Outline each uninfected red blood cell.
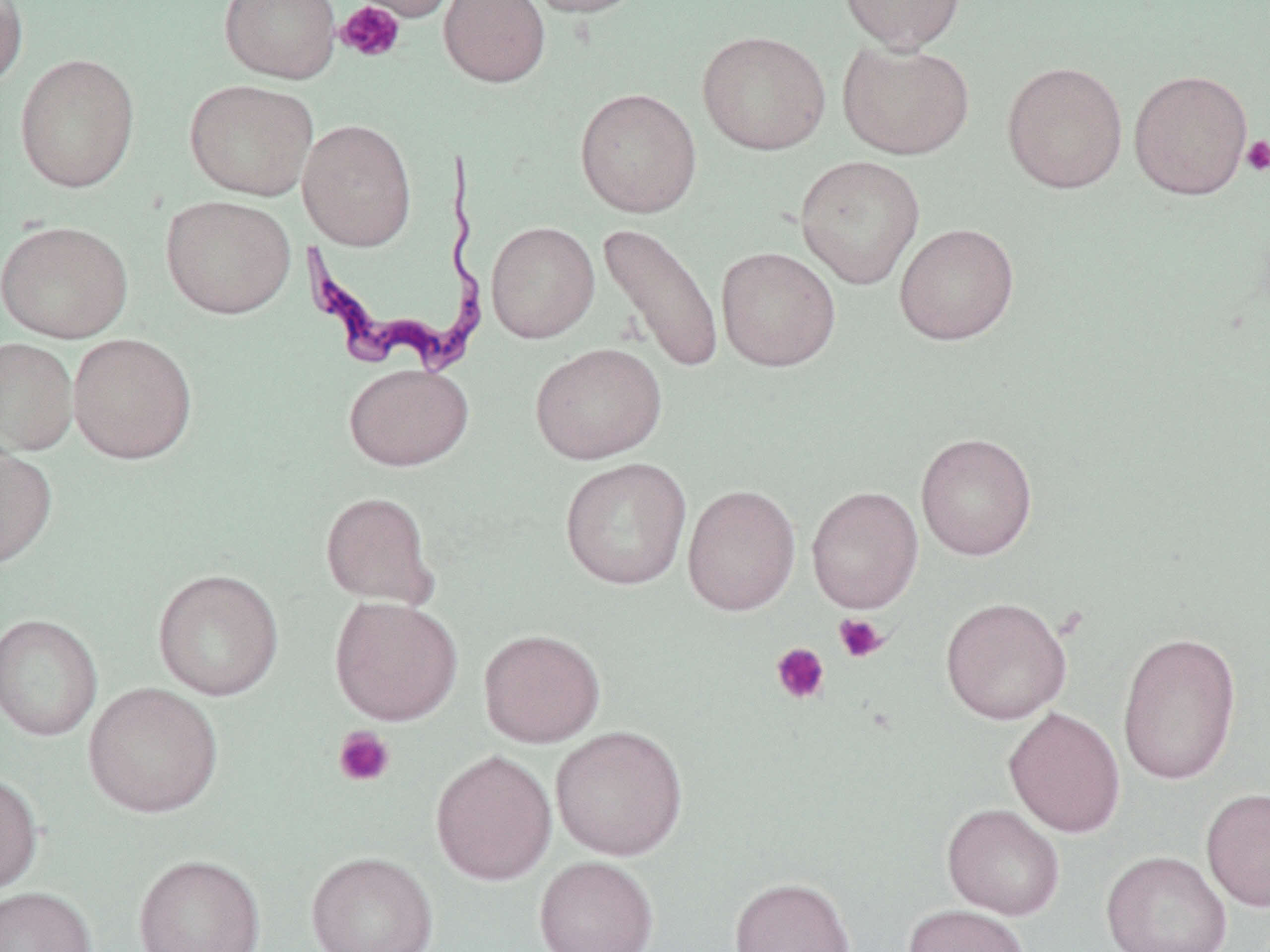

Approximate bounding boxes as named x1/y1/x2/y2 corners in pixels.
Uninfected red blood cells: (x1=0, y1=0, x2=29, y2=90), (x1=218, y1=0, x2=341, y2=83), (x1=347, y1=0, x2=460, y2=22), (x1=438, y1=0, x2=551, y2=89), (x1=521, y1=0, x2=649, y2=18), (x1=837, y1=0, x2=967, y2=52), (x1=697, y1=30, x2=831, y2=155), (x1=837, y1=40, x2=975, y2=159), (x1=15, y1=52, x2=141, y2=193), (x1=1001, y1=60, x2=1128, y2=193), (x1=1129, y1=69, x2=1253, y2=200), (x1=184, y1=79, x2=318, y2=201), (x1=574, y1=87, x2=702, y2=218), (x1=297, y1=118, x2=417, y2=251), (x1=794, y1=155, x2=926, y2=289), (x1=160, y1=195, x2=296, y2=319), (x1=0, y1=220, x2=133, y2=343), (x1=486, y1=221, x2=599, y2=343), (x1=596, y1=222, x2=725, y2=374), (x1=894, y1=223, x2=1019, y2=345), (x1=716, y1=246, x2=840, y2=371), (x1=68, y1=333, x2=198, y2=464), (x1=0, y1=337, x2=79, y2=457), (x1=530, y1=342, x2=667, y2=464), (x1=343, y1=363, x2=474, y2=471), (x1=916, y1=432, x2=1038, y2=560), (x1=0, y1=441, x2=57, y2=570), (x1=560, y1=457, x2=692, y2=590), (x1=682, y1=483, x2=802, y2=615), (x1=806, y1=486, x2=924, y2=613), (x1=319, y1=491, x2=439, y2=609), (x1=152, y1=568, x2=284, y2=700), (x1=329, y1=595, x2=463, y2=725), (x1=940, y1=596, x2=1072, y2=725), (x1=0, y1=613, x2=102, y2=741), (x1=479, y1=628, x2=605, y2=748), (x1=1116, y1=632, x2=1242, y2=785), (x1=83, y1=682, x2=223, y2=819), (x1=1003, y1=707, x2=1125, y2=838), (x1=550, y1=725, x2=688, y2=861), (x1=430, y1=749, x2=556, y2=885), (x1=0, y1=772, x2=43, y2=895), (x1=1201, y1=787, x2=1270, y2=912), (x1=942, y1=803, x2=1065, y2=920), (x1=1101, y1=850, x2=1232, y2=952), (x1=305, y1=851, x2=439, y2=952), (x1=134, y1=854, x2=265, y2=951), (x1=534, y1=856, x2=659, y2=951), (x1=729, y1=876, x2=856, y2=952), (x1=0, y1=886, x2=96, y2=952), (x1=903, y1=904, x2=1031, y2=952).

Summary:
  - Trypanosoma brucei locations: (x1=301, y1=149, x2=493, y2=382)
  - Platelet locations: (x1=335, y1=1, x2=405, y2=62), (x1=1240, y1=135, x2=1270, y2=176), (x1=833, y1=613, x2=889, y2=663), (x1=770, y1=642, x2=830, y2=705), (x1=333, y1=726, x2=395, y2=788)
  - Slide-level diagnosis: Trypanosoma brucei
  - Image size: 1270×952 pixels
  - Magnification: 1000x
  - Stain: May-Grünwald-Giemsa
  - Modality: optical microscopy
  - Preparation: thin blood smear
  - Field of view: single